Comment on the morphology of the erythrocytes.
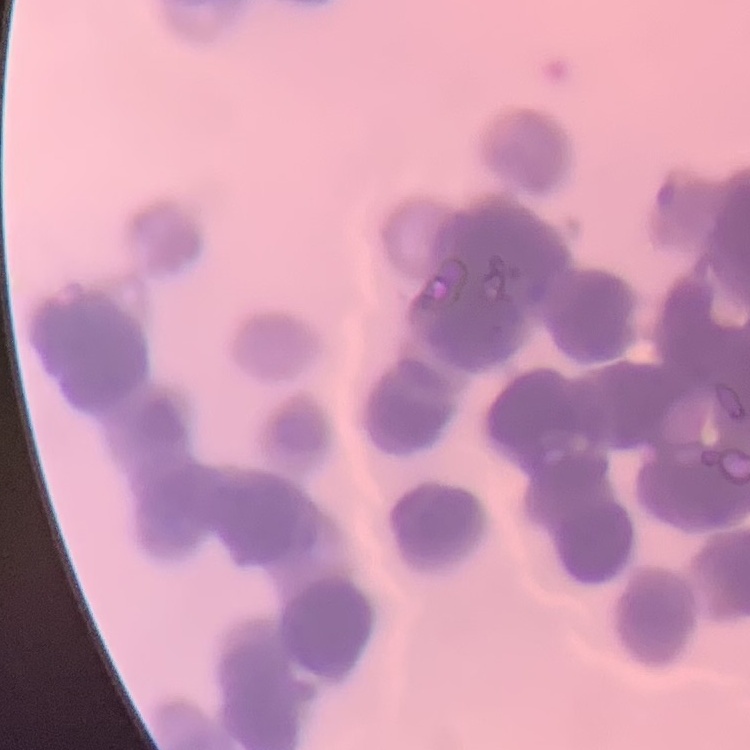

They show rouleaux formation.

Summary:
  - Image type: square crop of a larger photomicrograph
  - Stain: Field's or Giemsa
  - Preparation: thin blood film